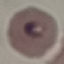

Summary:
  - Result: malaria parasites identified
  - Image type: automatically extracted cell patch, resized to 64 × 64 pixels
  - Preparation: thin smear
  - Capture: smartphone camera at the microscope eyepiece
  - Stain: Giemsa